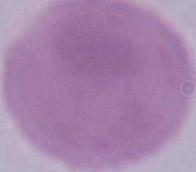
identification: red blood cell
modality: photomicrograph
magnification: 1000x